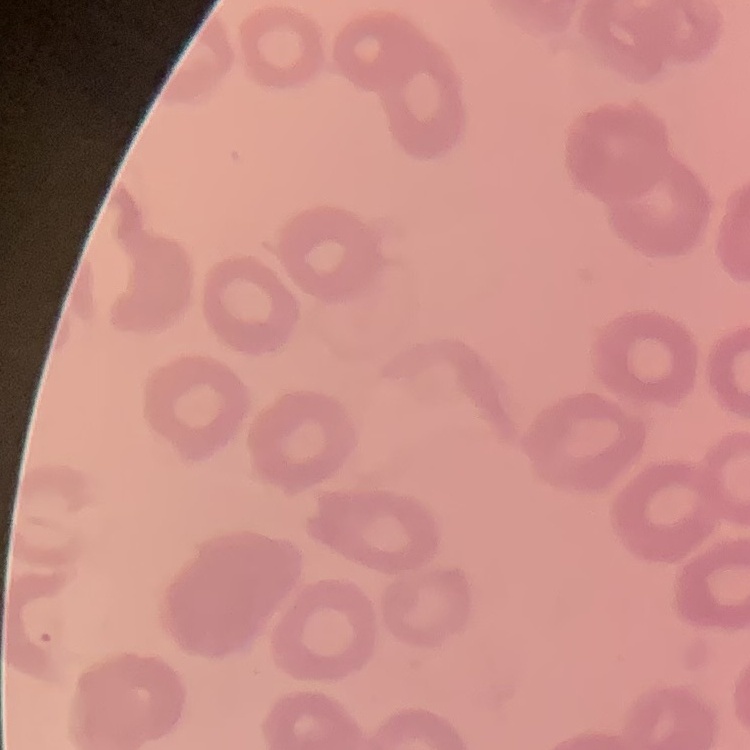

red blood cell morphology = no rouleaux formation
stain = Field's or Giemsa
image type = one tile cut from a larger photomicrograph
preparation = thin blood film